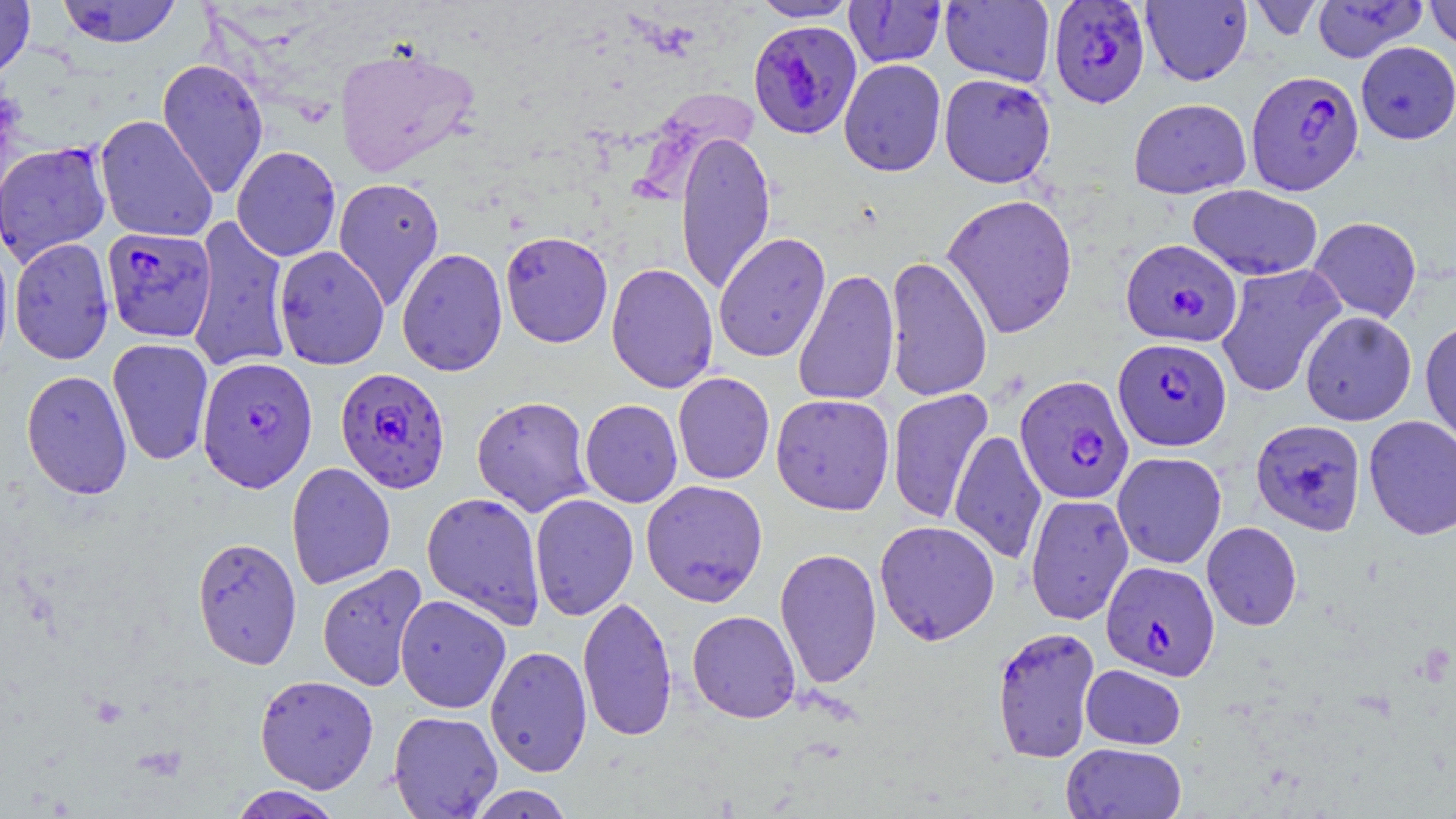 Approximate bounding boxes as [x1, y1, x2, y2] in pixels. Plasmodium falciparum-infected red blood cell locations: [1048, 1, 1151, 107], [748, 19, 863, 139], [1246, 69, 1364, 195], [0, 141, 112, 266], [101, 227, 216, 343], [1121, 239, 1242, 347], [1113, 337, 1232, 451], [197, 356, 318, 493], [334, 367, 451, 493], [1015, 375, 1134, 505], [1251, 419, 1366, 537], [1101, 560, 1220, 681], [992, 626, 1101, 762]. Uninfected red blood cell locations: [55, 0, 183, 48], [751, 0, 858, 22], [1141, 0, 1252, 86], [1248, 0, 1324, 40], [1311, 0, 1427, 62], [1424, 0, 1456, 51], [0, 1, 35, 80], [844, 1, 946, 68], [940, 1, 1055, 86], [1356, 41, 1455, 144], [333, 43, 480, 178], [156, 58, 269, 199], [839, 60, 946, 177], [939, 73, 1056, 188], [1128, 98, 1251, 199], [94, 115, 218, 243], [674, 130, 776, 296], [231, 145, 341, 261], [332, 177, 445, 310], [1187, 184, 1323, 280], [941, 192, 1078, 339], [186, 216, 293, 374], [1308, 216, 1421, 323], [500, 230, 614, 348], [713, 232, 831, 363], [0, 235, 13, 374], [9, 237, 114, 364], [273, 246, 390, 369], [396, 247, 508, 376], [884, 255, 993, 402], [606, 262, 719, 393], [1216, 264, 1346, 398], [793, 268, 900, 406], [1300, 311, 1416, 426], [1420, 320, 1456, 448], [107, 337, 214, 466], [21, 369, 133, 499], [673, 372, 775, 485], [887, 389, 993, 524], [770, 394, 895, 515], [472, 395, 594, 516], [579, 399, 682, 508], [1363, 415, 1456, 540], [949, 428, 1047, 565], [1112, 451, 1227, 569], [286, 462, 396, 590], [641, 479, 768, 606], [421, 492, 546, 628], [530, 493, 639, 621], [1024, 493, 1134, 625], [874, 520, 1000, 645], [1202, 522, 1302, 631], [190, 536, 303, 670], [774, 547, 882, 689], [316, 563, 429, 692], [395, 594, 511, 713], [578, 595, 678, 742], [687, 610, 801, 723], [485, 645, 592, 777], [1081, 664, 1185, 750], [254, 674, 379, 793], [388, 711, 503, 818], [1061, 742, 1187, 818], [464, 784, 577, 819], [226, 786, 346, 818]. Slide-level diagnosis: Plasmodium falciparum. Thin blood film. May-Grünwald-Giemsa stain. Captured at 1000x magnification. Optical microscopy. Image is 1456×819 pixels. One field of a larger specimen.